Report the malaria status of this cell.
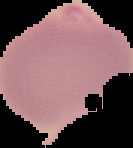

Parasitized.

image type = segmented cell region with the area outside set to black
preparation = thin blood film
image size = 133×148 pixels